Assess the morphology of the red blood cells.
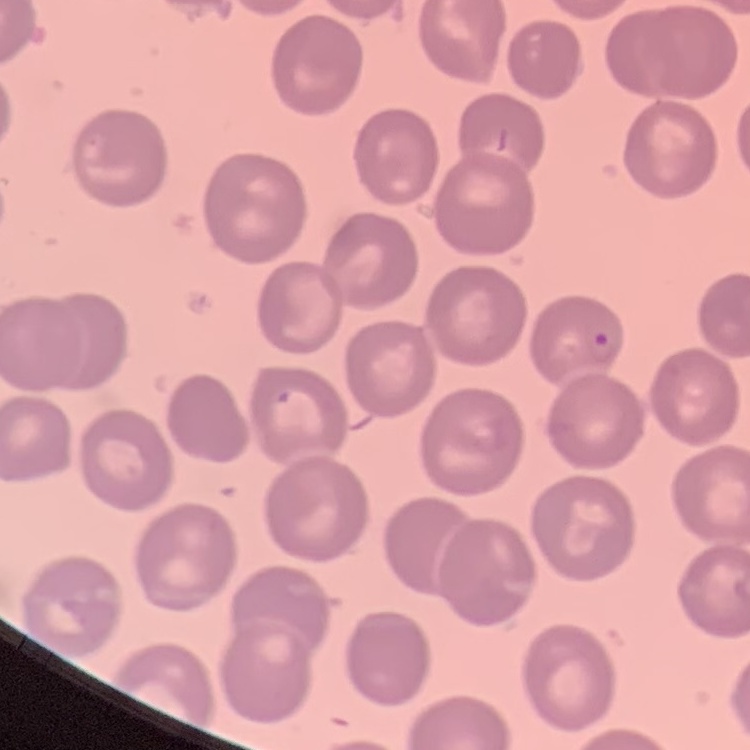

No rouleaux formation.

preparation = thin blood smear
stain = Field's or Giemsa
image type = square crop of a larger photomicrograph